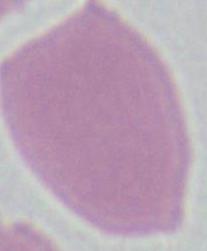

Summary:
  - Modality: micrograph
  - Magnification: 1000x
  - Identification: erythrocyte